Identify the parasite.
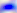

Toxoplasma gondii.

Summary:
  - Modality: micrograph
  - Magnification: 400x